Outline platelets.
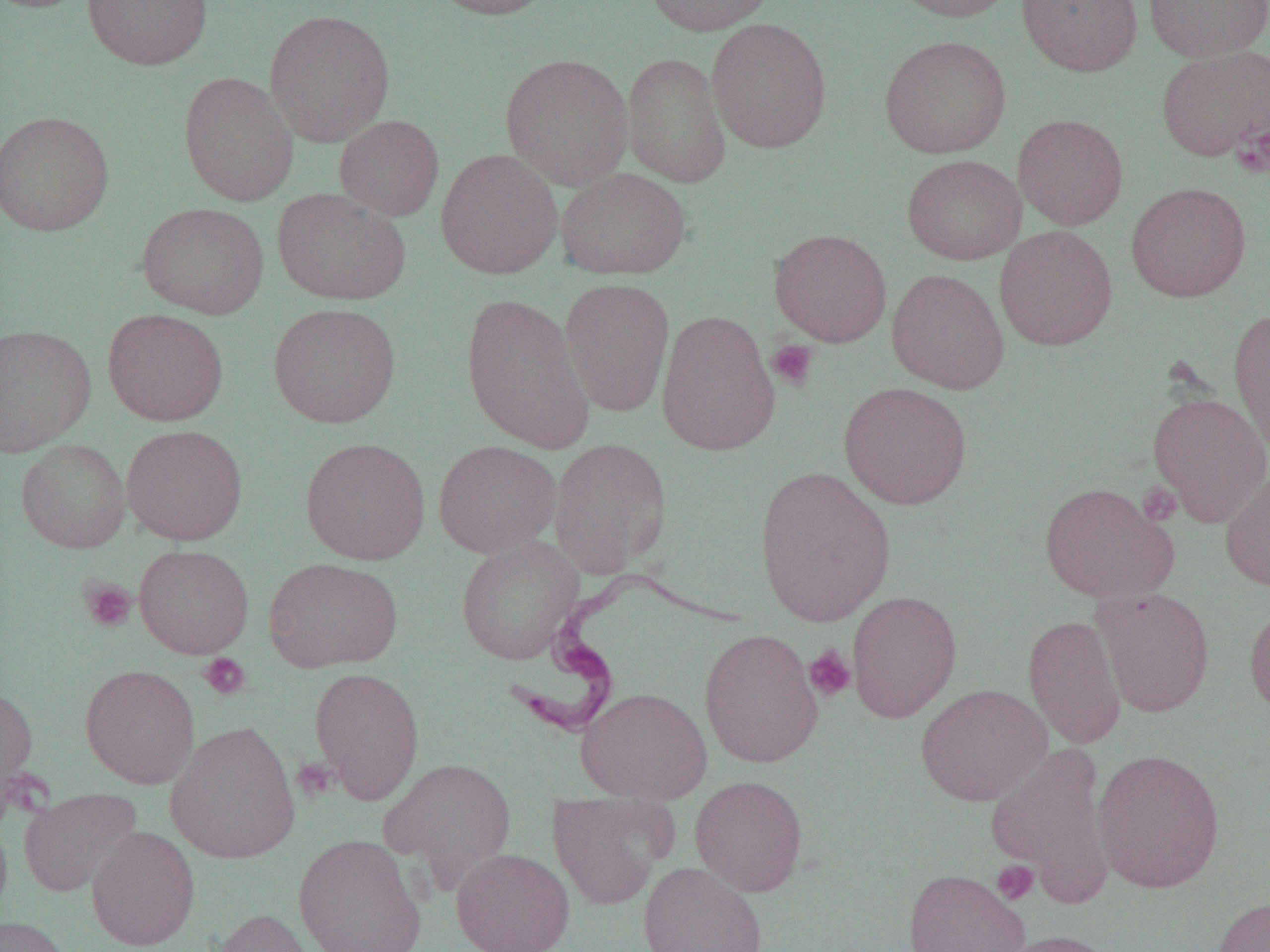

Approximate bounding boxes as (x1, y1, x2, y2) in pixels.
Platelets: (1232, 123, 1270, 179), (766, 340, 818, 391), (1137, 482, 1182, 526), (79, 578, 137, 633), (803, 645, 857, 702), (198, 653, 251, 700), (292, 758, 338, 801), (992, 860, 1039, 905).

Uninfected red blood cell locations: (0, 0, 91, 13), (82, 0, 212, 70), (428, 0, 558, 19), (643, 0, 778, 35), (889, 0, 1021, 22), (1017, 0, 1143, 77), (1143, 0, 1269, 62), (264, 9, 395, 147), (706, 18, 832, 153), (879, 35, 1011, 158), (1156, 45, 1270, 161), (500, 52, 633, 189), (622, 52, 731, 188), (178, 71, 298, 206), (0, 110, 114, 237), (1013, 114, 1128, 230), (335, 115, 444, 220), (435, 148, 563, 279), (902, 154, 1026, 265), (556, 168, 691, 280), (1126, 183, 1252, 302), (272, 188, 412, 305), (137, 202, 269, 319), (995, 225, 1118, 351), (769, 228, 892, 347), (887, 268, 1009, 394), (559, 277, 674, 417), (460, 293, 596, 453), (268, 303, 401, 428), (1228, 307, 1270, 456), (103, 308, 228, 426), (657, 309, 779, 457), (0, 324, 96, 457), (838, 382, 972, 509), (1148, 392, 1270, 526), (121, 425, 248, 546), (300, 437, 431, 565), (548, 438, 671, 576), (17, 439, 130, 553), (433, 439, 562, 558), (753, 465, 897, 625), (1221, 469, 1270, 592), (1039, 482, 1178, 604), (456, 536, 584, 665), (134, 544, 254, 658), (264, 557, 403, 672), (1090, 587, 1215, 717), (847, 590, 962, 723), (1244, 599, 1270, 719), (1023, 615, 1126, 750), (699, 628, 824, 768), (80, 664, 200, 789), (309, 666, 424, 804), (916, 684, 1052, 806), (0, 685, 38, 812), (576, 687, 712, 804), (165, 720, 301, 865), (985, 744, 1117, 905), (1092, 748, 1225, 894), (379, 758, 516, 886), (689, 774, 808, 896), (19, 788, 142, 897), (548, 792, 678, 910), (86, 826, 200, 950), (293, 833, 427, 952), (451, 847, 574, 952), (636, 861, 769, 952), (903, 868, 1031, 952), (1213, 896, 1270, 952), (211, 908, 323, 952), (0, 916, 72, 952), (993, 930, 1125, 952). Trypanosoma brucei locations: (505, 566, 750, 739). Slide-level diagnosis: Trypanosoma brucei. One field of a larger specimen. Thin blood smear. Light microscopy. Image is 1270×952 pixels. 1000x magnification.